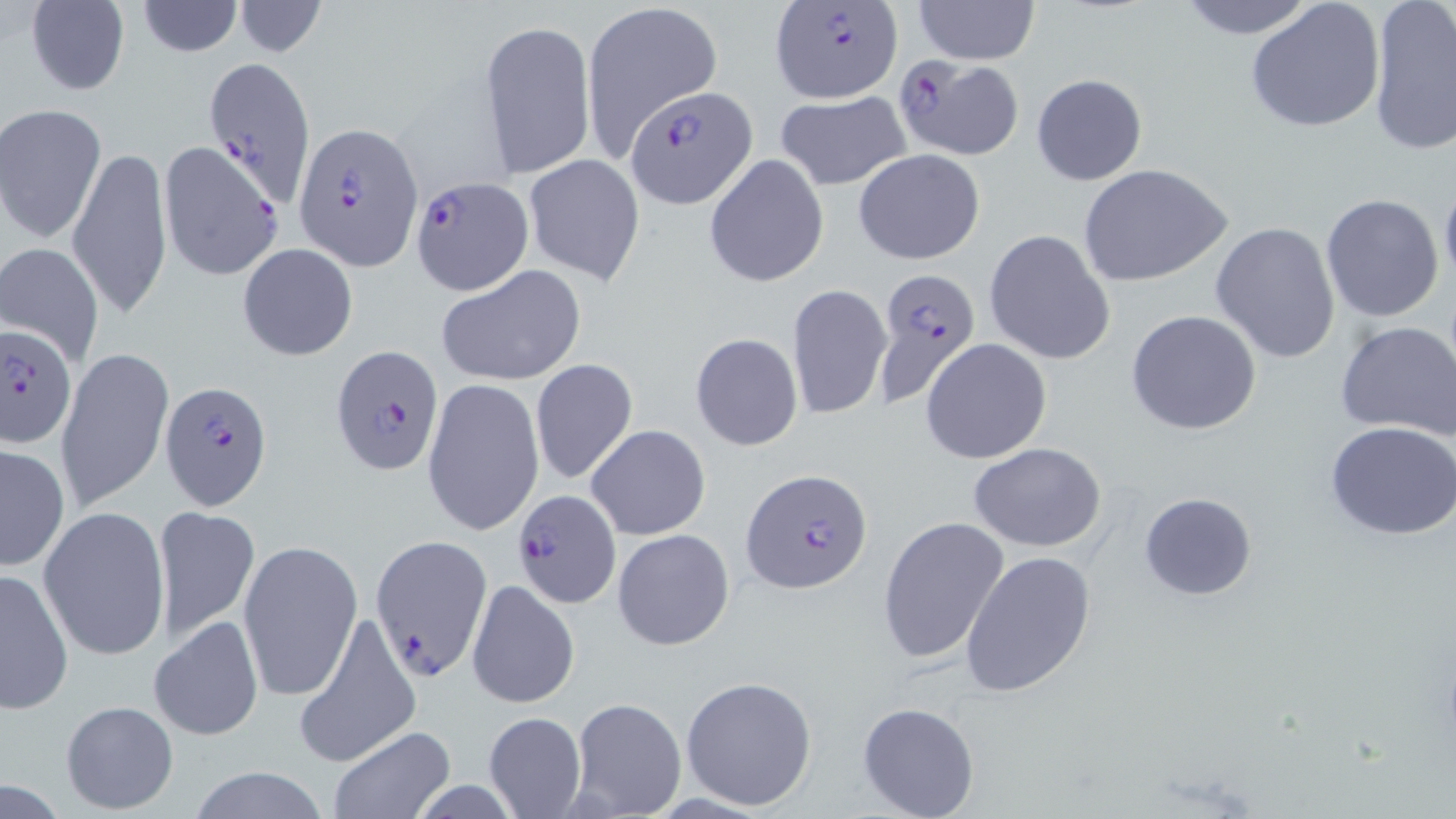
Plasmodium falciparum-infected red blood cell locations = approximate bounding boxes as (x1, y1, x2, y2) in pixels: (768, 3, 904, 104), (204, 56, 321, 210), (890, 56, 1026, 158), (626, 86, 756, 211), (292, 122, 423, 272), (410, 174, 532, 294), (872, 270, 982, 404), (0, 325, 75, 447), (331, 346, 443, 476), (158, 380, 273, 509), (741, 467, 873, 595), (511, 489, 624, 610), (371, 535, 491, 681)
slide-level diagnosis = Plasmodium falciparum
stain = May-Grünwald-Giemsa
uninfected red blood cell locations = approximate bounding boxes as (x1, y1, x2, y2) in pixels: (580, 0, 723, 157), (912, 0, 1041, 66), (1170, 0, 1323, 39), (24, 1, 131, 97), (135, 1, 244, 57), (233, 1, 326, 58), (1245, 1, 1386, 136), (1367, 1, 1456, 155), (479, 18, 595, 179), (1031, 73, 1148, 187), (774, 91, 911, 191), (2, 105, 109, 243), (157, 140, 283, 284), (69, 144, 174, 319), (852, 150, 986, 263), (524, 153, 645, 286), (704, 153, 829, 288), (1077, 163, 1232, 288), (1439, 177, 1456, 295), (1319, 193, 1446, 324), (1211, 222, 1343, 363), (984, 228, 1116, 365), (237, 242, 358, 360), (2, 244, 104, 366), (436, 264, 588, 386), (786, 283, 892, 421), (1125, 309, 1262, 435), (1334, 320, 1456, 443), (690, 333, 803, 451), (920, 338, 1053, 465), (55, 345, 174, 512), (530, 358, 638, 486), (422, 377, 545, 537), (1325, 420, 1456, 539), (587, 425, 711, 540), (968, 442, 1107, 553), (0, 443, 69, 571), (1138, 492, 1256, 601), (38, 505, 169, 661), (151, 505, 261, 645), (877, 516, 1009, 665), (612, 529, 735, 650), (238, 538, 363, 704), (959, 550, 1098, 698), (1, 567, 74, 712), (467, 579, 580, 710), (292, 611, 420, 770), (150, 616, 264, 742), (680, 675, 818, 811), (569, 697, 687, 818), (59, 699, 180, 813), (856, 700, 980, 818), (482, 712, 585, 819), (328, 725, 455, 817), (184, 766, 332, 819)
field of view = one of a larger specimen
preparation = thin blood film
modality = light microscopy
magnification = 1000x
image size = 1456×819 pixels